Report the malaria status of this cell.
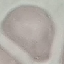

It is uninfected.

{
  "image_type": "automatically extracted cell patch, resized to 64 × 64 pixels",
  "preparation": "thin blood film",
  "capture": "smartphone camera at the microscope eyepiece",
  "stain": "Giemsa"
}